Assess the morphology of the red blood cells.
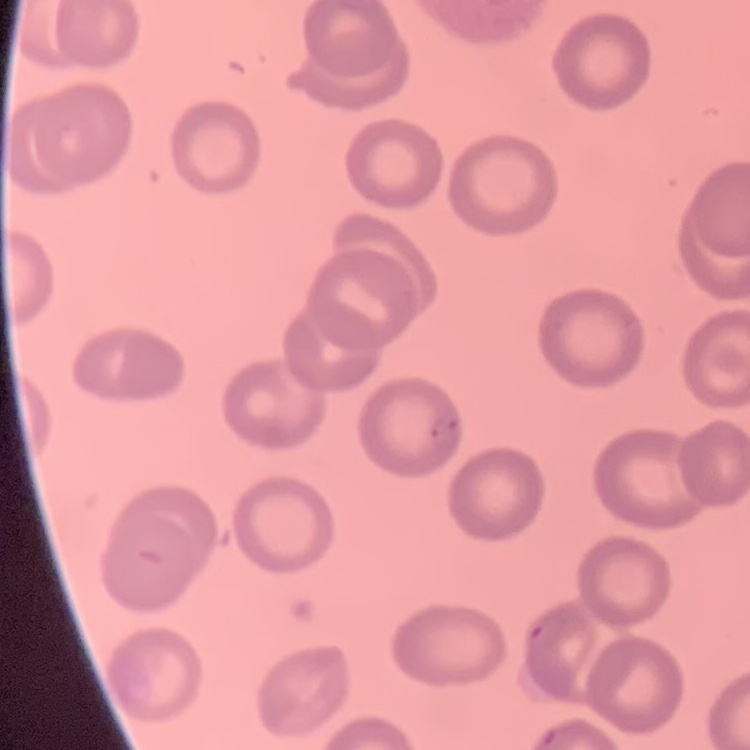
They show no rouleaux formation.

Summary:
  - Stain: Field's or Giemsa
  - Preparation: thin blood film
  - Image type: square crop of a larger photomicrograph